Give the position of every leukocyte visible.
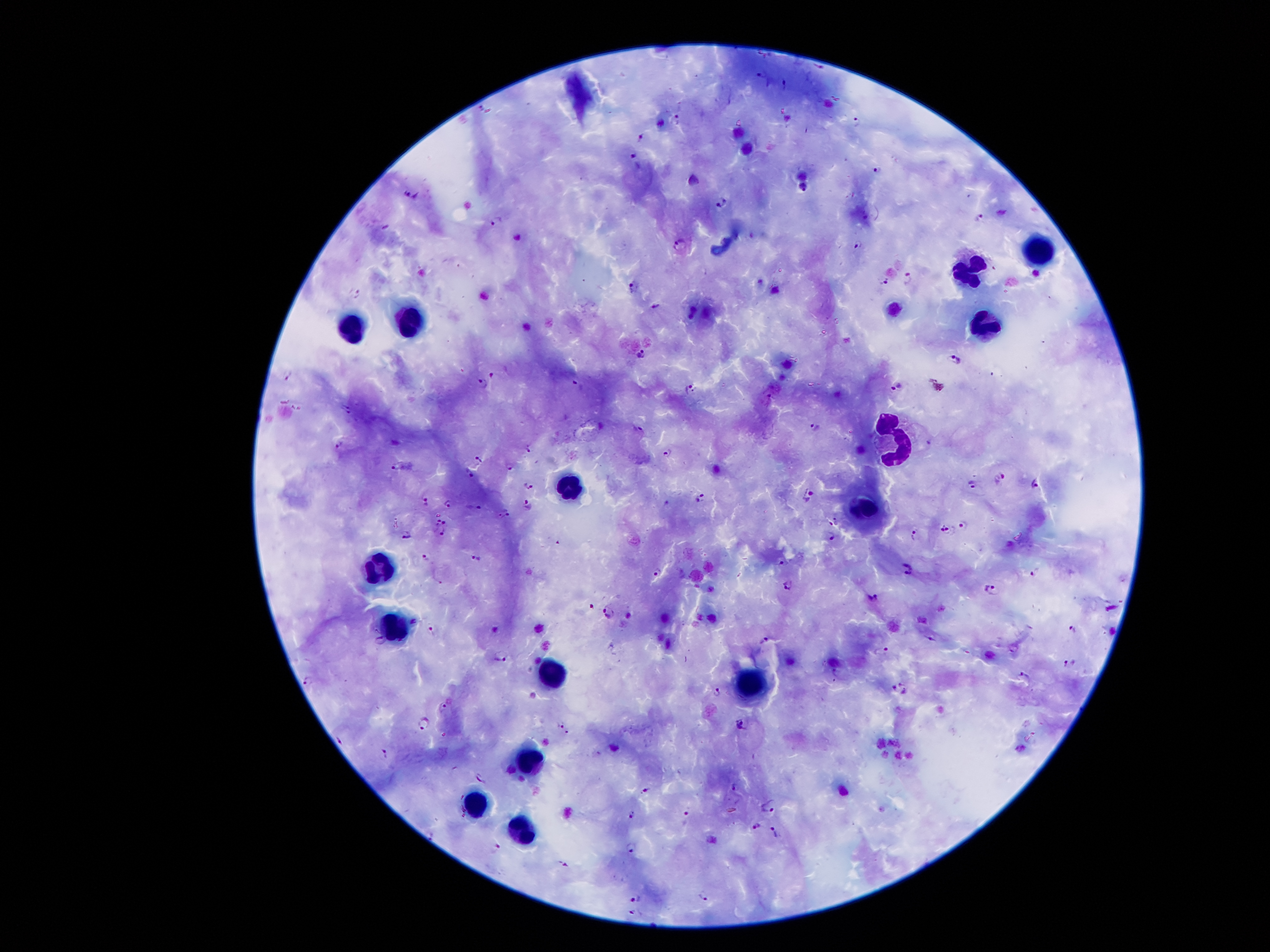
Approximate centers as {x, y} in pixels.
Leukocytes: {1037, 249}, {969, 271}, {986, 322}, {352, 325}, {406, 326}, {895, 436}, {568, 488}, {868, 507}, {382, 568}, {392, 624}, {552, 678}, {754, 681}, {529, 759}, {473, 806}, {520, 827}.

Summary:
  - Plasmodium parasite locations: {482, 107}, {676, 117}, {856, 121}, {641, 135}, {634, 154}, {877, 169}, {411, 193}, {721, 201}, {979, 216}, {498, 220}, {681, 244}, {858, 244}, {909, 277}, {886, 279}, {633, 286}, {355, 294}, {655, 306}, {642, 353}, {955, 360}, {287, 374}, {492, 375}, {483, 384}, {896, 385}, {578, 386}, {688, 388}, {770, 396}, {347, 403}, {345, 414}, {816, 424}, {639, 429}, {339, 445}, {527, 449}, {668, 452}, {479, 459}, {510, 465}, {394, 467}, {469, 472}, {999, 477}, {972, 483}, {529, 484}, {1036, 484}, {808, 495}, {701, 497}, {425, 502}, {448, 504}, {527, 504}, {474, 507}, {507, 512}, {501, 516}, {835, 518}, {444, 522}, {964, 524}, {441, 529}, {948, 529}, {914, 533}, {406, 534}, {831, 536}, {477, 557}, {426, 558}, {783, 562}, {909, 570}, {658, 571}, {1035, 571}, {789, 584}, {991, 588}, {875, 596}, {590, 606}, {608, 611}, {433, 628}, {1071, 628}, {765, 639}, {380, 640}, {881, 650}, {502, 656}, {1067, 663}, {1022, 676}, {307, 682}, {900, 688}, {716, 691}, {442, 705}, {424, 721}, {561, 723}, {741, 724}, {567, 731}, {385, 751}, {480, 778}, {734, 787}, {647, 791}, {770, 807}, {632, 815}, {687, 816}, {756, 825}, {774, 830}, {494, 847}, {632, 847}, {563, 865}, {702, 894}, {634, 897}, {637, 913}
  - Preparation: thick peripheral-blood smear
  - Stain: Giemsa
  - Capture: smartphone through the microscope eyepiece
  - Magnification: 100x
  - Image size: 1270×952 pixels
  - Patient malaria status: positive for Plasmodium falciparum
  - Field of view: one from this slide